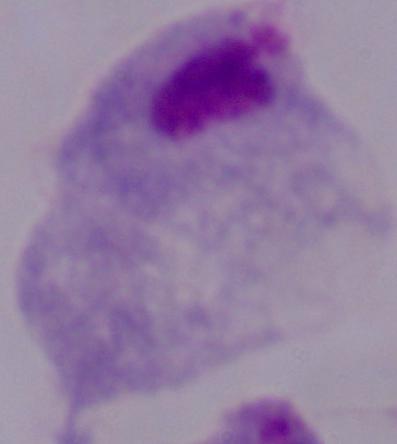 Captured at 1000x magnification. A trichomonad is seen. Photomicrograph.